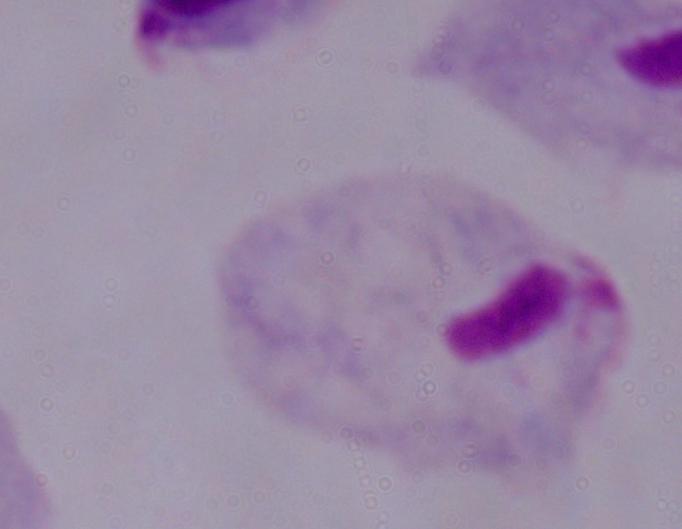

Summary:
  - Identification: trichomonad
  - Magnification: 1000x
  - Modality: micrograph